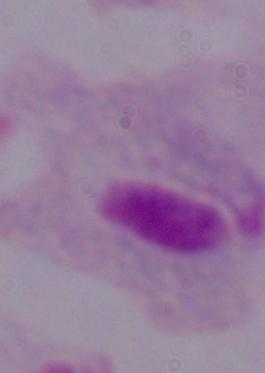

identification: trichomonad
modality: photomicrograph
magnification: 1000x